Classify this cell by malaria status.
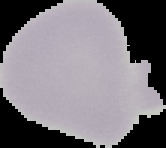
Uninfected.

image_size: 166×148 pixels
preparation: thin blood smear
image_type: cell region segmented out of the field of view; surrounding area masked to black